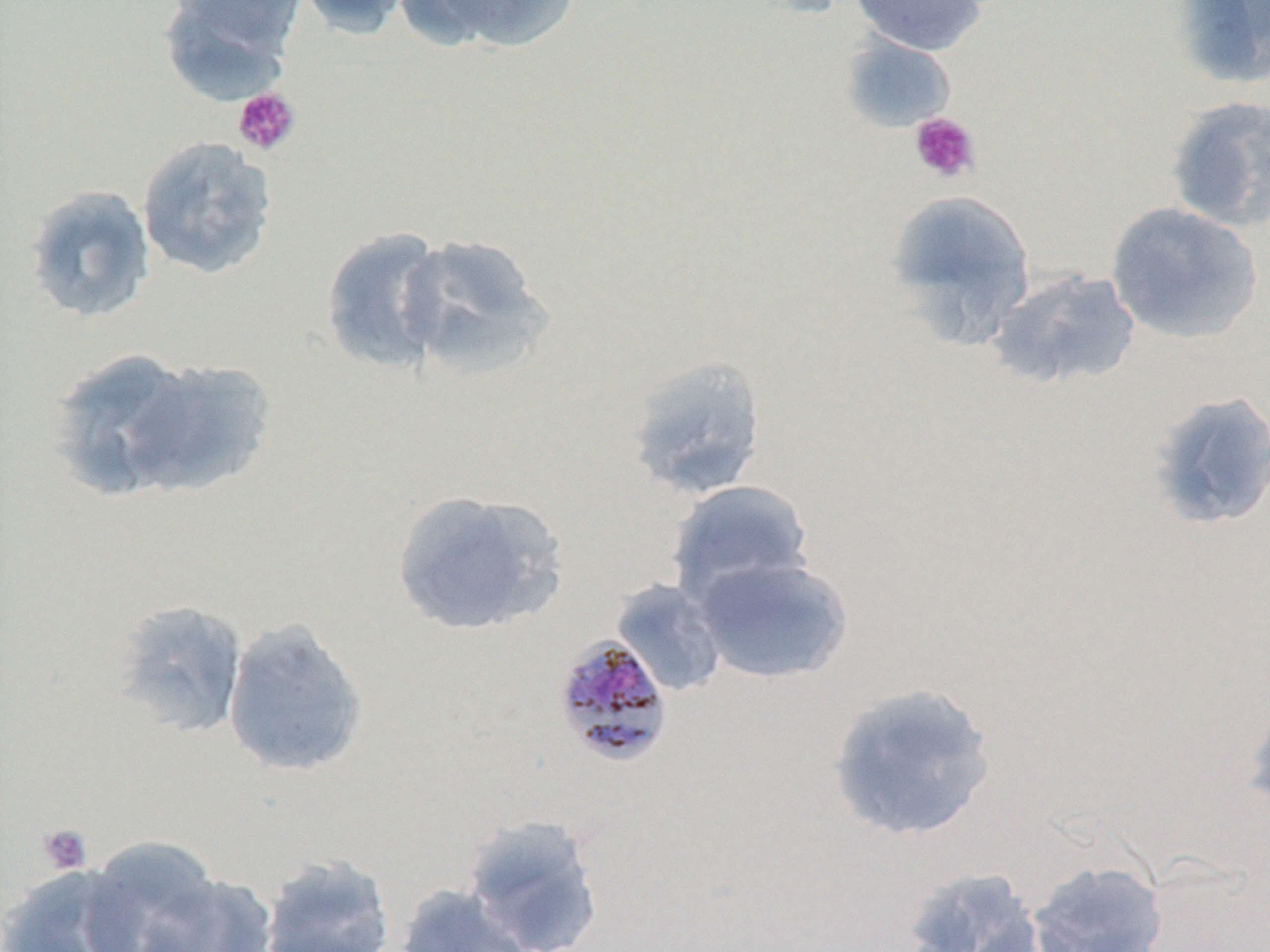

Approximate bounding boxes as (x1,y1)-(x2,y2) corner pairs in pixels. Uninfected red blood cell locations: (294,0)-(414,40), (410,0)-(579,54), (849,0)-(988,56), (1174,0)-(1270,87), (160,1)-(297,105), (840,35)-(956,133), (1165,96)-(1270,232), (136,135)-(278,281), (23,184)-(157,325), (884,189)-(1037,349), (1105,202)-(1263,344), (319,226)-(450,374), (396,232)-(552,381), (987,268)-(1142,392), (45,347)-(206,503), (623,354)-(767,501), (118,357)-(276,499), (1146,391)-(1270,531), (666,479)-(816,606), (390,489)-(568,638), (692,555)-(854,685), (610,579)-(729,697), (108,599)-(249,740), (222,618)-(369,778), (826,682)-(998,843), (1242,690)-(1270,824), (461,813)-(607,952), (78,835)-(231,952), (259,854)-(395,951), (1026,859)-(1169,951), (0,865)-(140,952), (899,865)-(1047,952), (131,870)-(280,952), (393,883)-(536,952). Plasmodium malariae-infected red blood cell locations: (551,634)-(674,768). Platelet locations: (232,87)-(301,156), (908,112)-(981,184), (36,823)-(93,875). Slide-level diagnosis: Plasmodium malariae. Thin blood smear. Light microscopy. Captured at 1000x magnification. May-Grünwald-Giemsa stain. One field of a larger specimen. Image is 1270×952 pixels.